State which parasite is depicted.
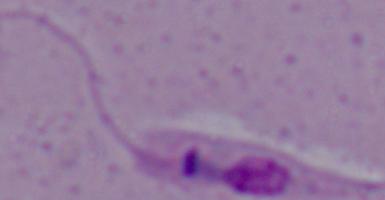
This is Leishmania.

Summary:
  - Magnification: 1000x
  - Modality: photomicrograph